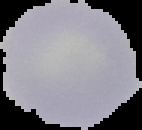
Summary:
  - Image size: 142×130 pixels
  - Image type: cell region segmented out of the field of view; surrounding area masked to black
  - Preparation: thin blood smear
  - Malaria status: uninfected